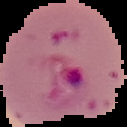

image size = 127×127 pixels
preparation = thin blood smear
image type = segmented cell region on a black background
result = malaria parasites detected